Comment on the morphology of the erythrocytes.
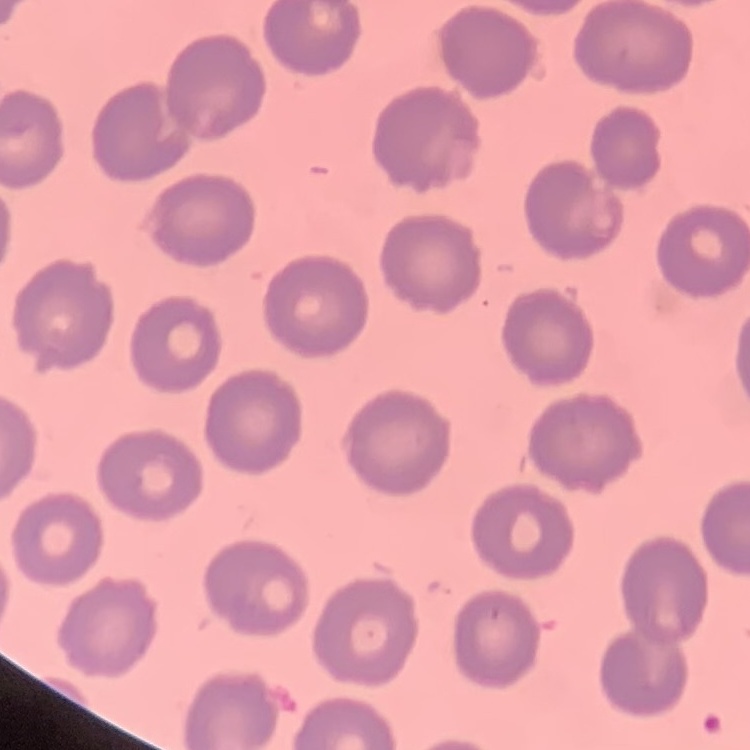

No rouleaux formation.

Summary:
  - Preparation: thin blood film
  - Image type: square crop of a larger photomicrograph
  - Stain: Field's or Giemsa